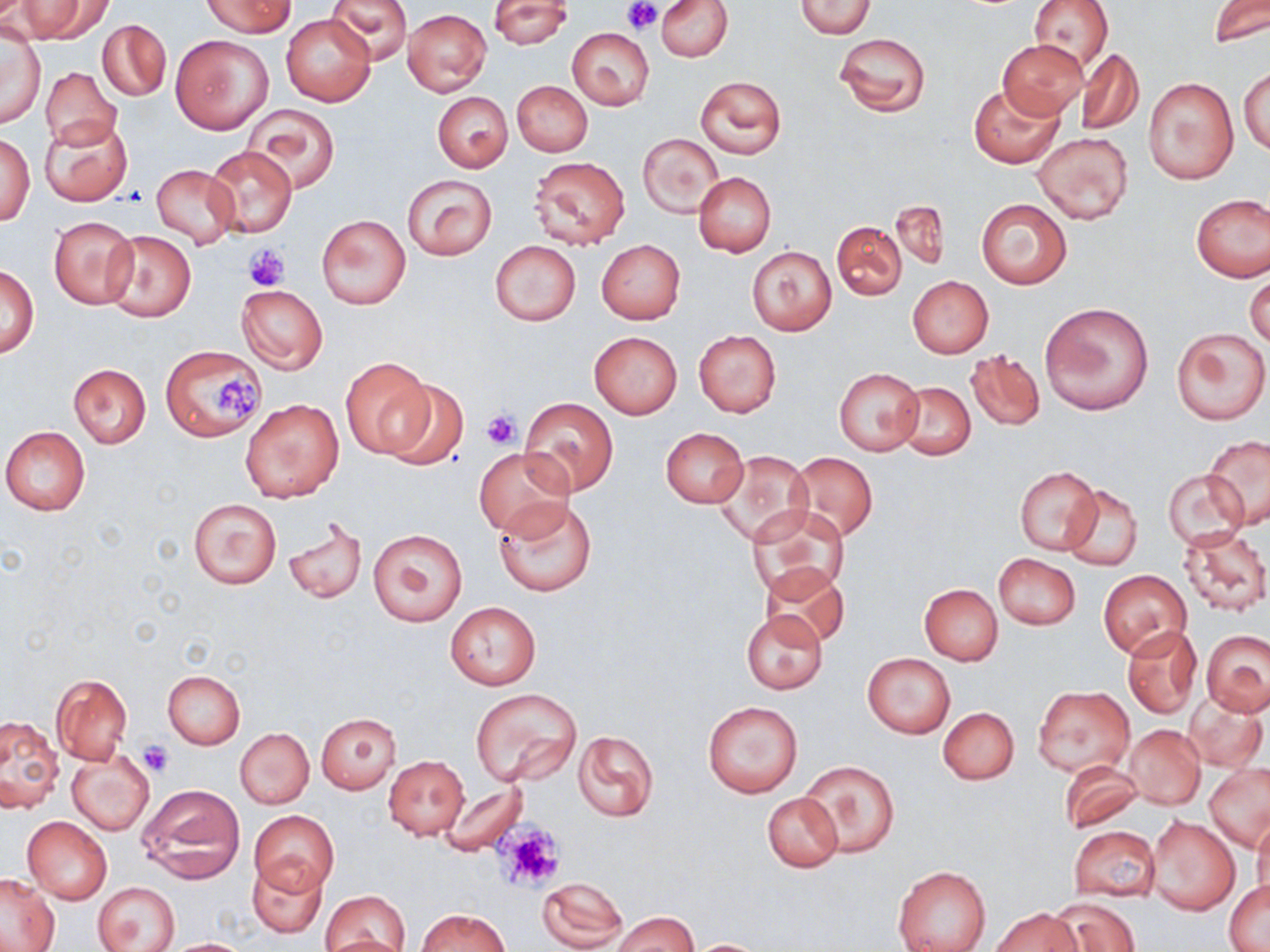
Approximate bounding boxes as [x1, y1, x2, y2] in pixels. Uninfected red blood cell locations: [19, 0, 112, 43], [203, 0, 291, 37], [326, 0, 412, 64], [657, 0, 733, 62], [1028, 0, 1114, 72], [1207, 0, 1269, 47], [488, 1, 572, 49], [797, 1, 875, 38], [402, 9, 491, 96], [281, 14, 375, 106], [98, 20, 170, 101], [568, 27, 654, 110], [1, 31, 45, 128], [833, 32, 931, 118], [171, 36, 272, 134], [998, 39, 1087, 119], [1077, 49, 1143, 136], [1240, 64, 1269, 157], [41, 67, 121, 151], [696, 74, 787, 159], [1144, 77, 1238, 184], [512, 81, 591, 156], [971, 84, 1062, 167], [433, 92, 512, 172], [243, 103, 340, 194], [40, 117, 132, 206], [2, 131, 34, 226], [1034, 132, 1133, 224], [639, 134, 722, 217], [204, 145, 297, 238], [528, 156, 630, 249], [152, 164, 240, 247], [693, 172, 776, 257], [403, 174, 497, 261], [1192, 193, 1270, 283], [974, 197, 1072, 289], [890, 200, 949, 270], [316, 213, 412, 310], [48, 215, 140, 310], [831, 219, 906, 300], [103, 230, 196, 322], [595, 239, 685, 325], [491, 240, 580, 325], [747, 246, 836, 335], [1, 264, 39, 357], [1246, 272, 1269, 350], [907, 275, 993, 358], [236, 284, 328, 373], [1042, 301, 1155, 415], [1172, 326, 1269, 424], [692, 330, 781, 418], [589, 332, 682, 419], [161, 346, 267, 441], [966, 348, 1045, 431], [338, 356, 437, 459], [68, 363, 151, 447], [834, 368, 924, 455], [379, 378, 470, 470], [894, 381, 976, 459], [240, 398, 344, 502], [519, 399, 619, 497], [1, 426, 90, 515], [660, 427, 747, 508], [1202, 435, 1270, 530], [474, 446, 574, 539], [712, 449, 812, 547], [788, 452, 877, 541], [1014, 466, 1100, 555], [1163, 469, 1249, 550], [1059, 485, 1142, 571], [493, 496, 595, 597], [187, 498, 281, 589], [749, 505, 851, 601], [282, 515, 367, 604], [1178, 526, 1269, 616], [367, 527, 468, 627], [992, 552, 1080, 631], [758, 562, 849, 648], [1099, 570, 1192, 660], [920, 584, 1003, 665], [445, 602, 541, 689], [740, 609, 827, 694], [1122, 624, 1202, 718], [1202, 629, 1270, 716], [862, 654, 955, 738], [161, 670, 245, 749], [51, 673, 132, 764], [1033, 686, 1135, 777], [472, 688, 582, 787], [1185, 694, 1267, 772], [702, 700, 805, 798], [939, 707, 1019, 785], [316, 712, 401, 794], [0, 715, 64, 814], [1124, 725, 1205, 809], [234, 728, 314, 808], [573, 731, 659, 822], [68, 748, 155, 835], [383, 755, 469, 840], [799, 760, 900, 858], [1058, 760, 1142, 833], [1204, 764, 1270, 851], [436, 781, 527, 855], [136, 784, 247, 884], [762, 791, 843, 872], [249, 810, 338, 895], [1250, 812, 1270, 900], [1146, 815, 1240, 915], [22, 816, 112, 905], [1068, 824, 1161, 902], [246, 857, 327, 939], [892, 865, 990, 952], [1, 873, 59, 951], [535, 876, 628, 952], [94, 882, 179, 952], [1225, 882, 1269, 951], [321, 891, 409, 951], [1051, 897, 1140, 952], [991, 907, 1082, 952], [415, 908, 511, 952], [610, 911, 697, 952], [159, 938, 254, 951], [685, 938, 773, 951]. Platelet locations: [623, 0, 661, 34], [243, 243, 291, 290], [211, 376, 263, 415], [482, 410, 520, 449], [139, 740, 172, 776], [498, 822, 564, 889]. Slide-level diagnosis: negative for blood parasites. One field of a larger specimen. Image is 1270×952 pixels. Thin blood smear. May-Grünwald-Giemsa-stained preparation. Optical microscopy. 1000x magnification.